Assess this cell for malaria.
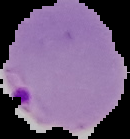

Parasitized.

preparation = thin blood smear
image size = 130×139 pixels
image type = segmented cell region with the area outside set to black